Evaluate for parasitized red blood cells.
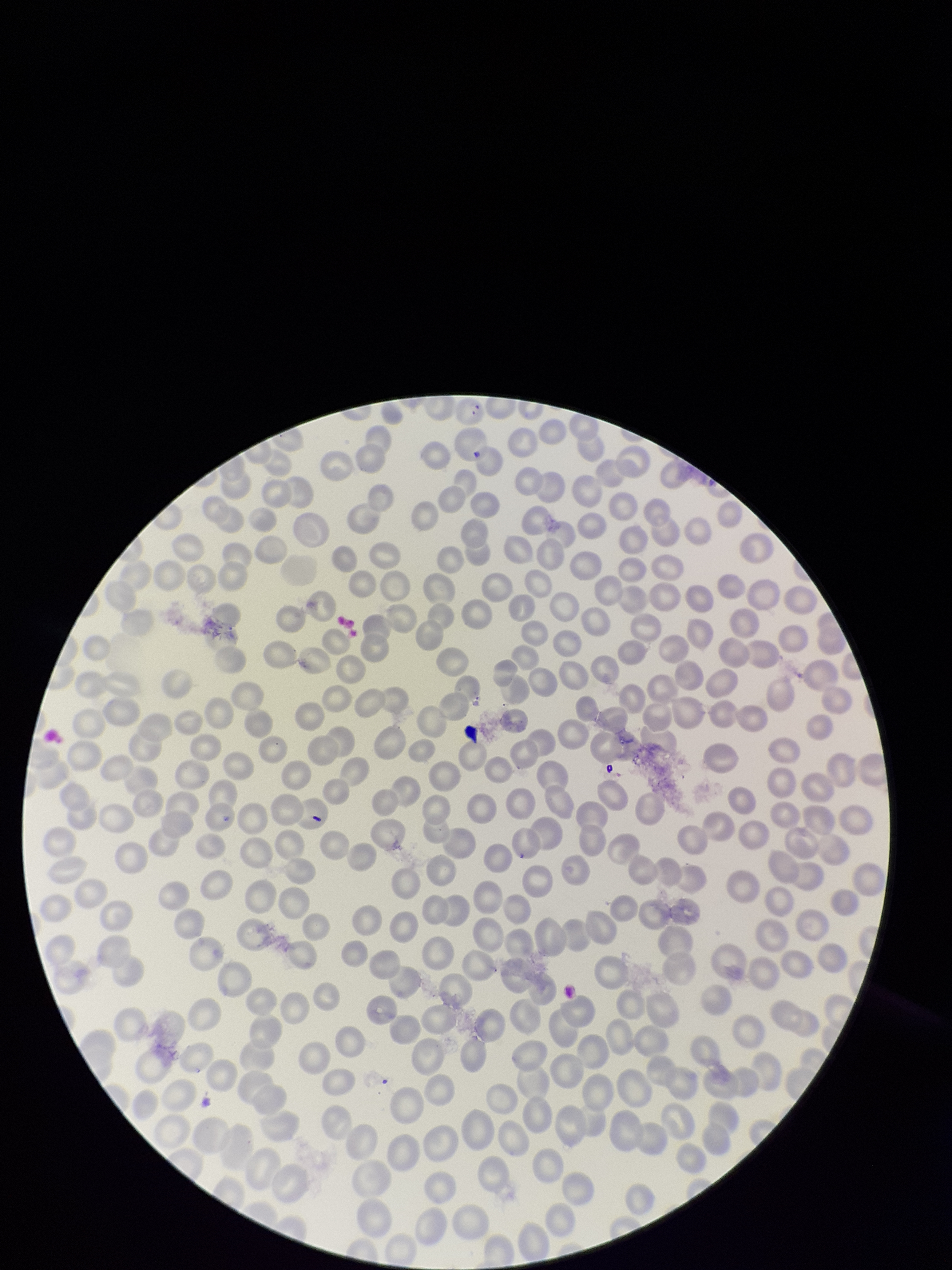
Identified.

{
  "capture": "smartphone photograph through the microscope eyepiece",
  "image_size": "952×1270 pixels",
  "preparation": "thin smear",
  "field_of_view": "one from this slide",
  "stain": "Giemsa",
  "species_reported_for_this_patient": "Plasmodium falciparum",
  "parasitized_red_blood_cell_count": 1,
  "red_blood_cell_count": 295,
  "patient_malaria_status": "positive"
}